Comment on the morphology of the red blood cells.
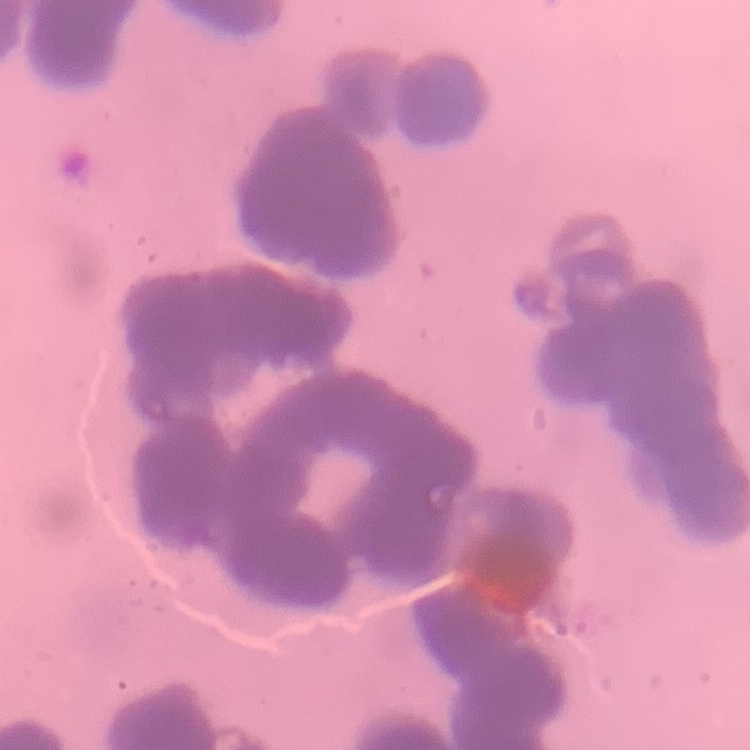

Rouleaux formation.

stain = Field's or Giemsa
image type = square crop of a larger photomicrograph
preparation = thin blood smear